Name the parasite shown.
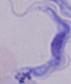
A trypanosome.

Photomicrograph. 1000x magnification.